Assess this cell for malaria.
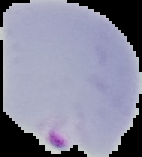
Parasitized.

Summary:
  - Image type: cell region segmented out of the field of view; surrounding area masked to black
  - Image size: 142×157 pixels
  - Preparation: thin blood smear